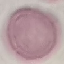

result = no malaria parasites seen
stain = Giemsa
capture = smartphone through the microscope eyepiece
preparation = thin blood film
image type = cell patch, automatically extracted from a larger field of view and resized to 64 × 64 pixels